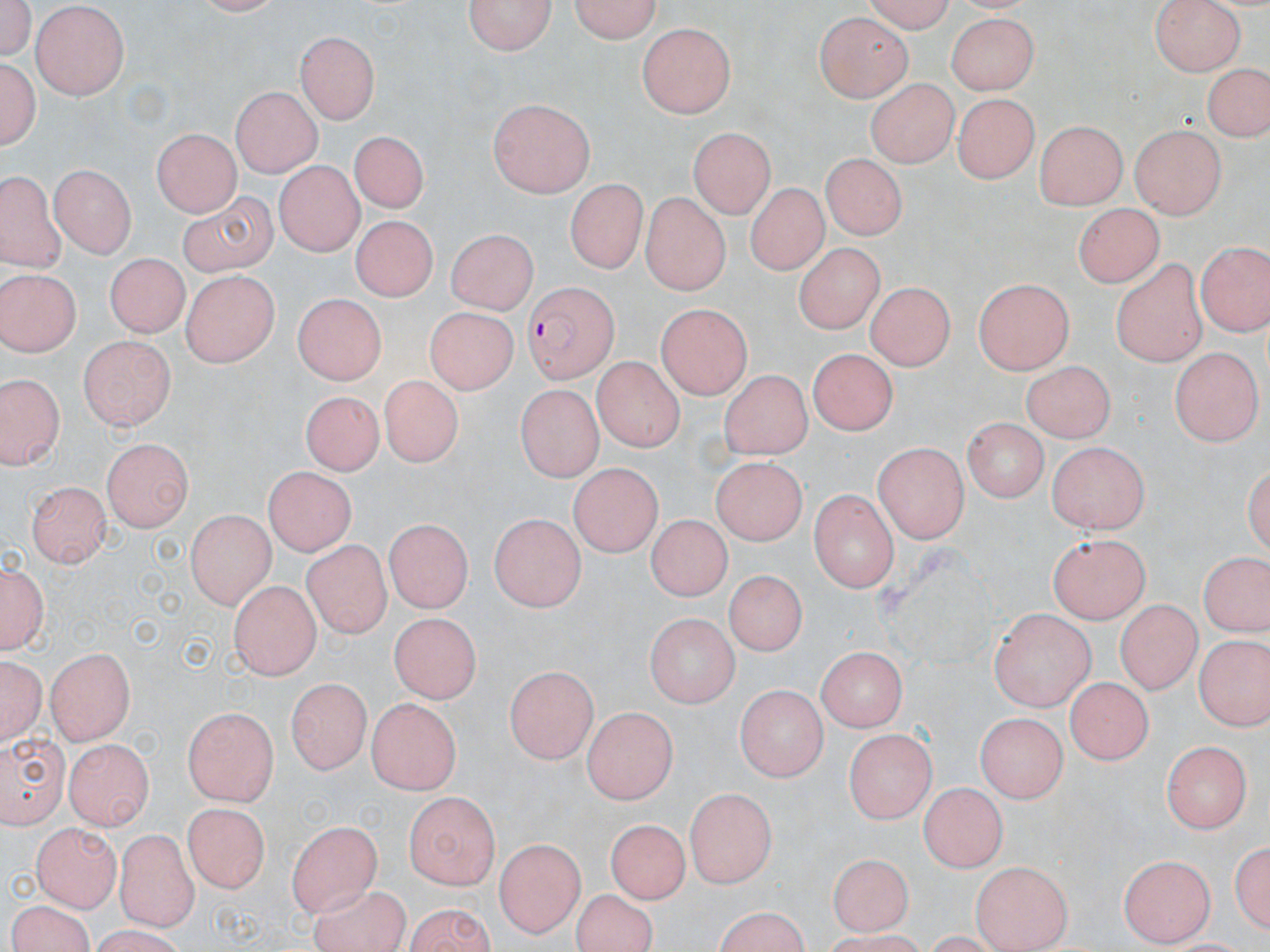

Summary:
  - Coordinate format: approximate bounding boxes as (x1,y1)-(x2,y2) corner pairs in pixels
  - Plasmodium falciparum-infected red blood cell locations: (523,282)-(617,384)
  - Uninfected red blood cell locations: (1,0)-(36,63), (467,0)-(555,57), (562,0)-(665,43), (858,0)-(958,29), (1150,0)-(1244,74), (32,5)-(134,100), (815,12)-(912,104), (944,13)-(1037,95), (637,26)-(737,119), (296,33)-(382,123), (2,56)-(40,154), (1207,61)-(1269,144), (866,76)-(956,167), (233,84)-(322,177), (956,94)-(1035,184), (489,100)-(597,199), (1036,121)-(1127,206), (1129,125)-(1229,219), (691,128)-(778,213), (149,129)-(241,216), (349,129)-(426,215), (823,153)-(905,243), (276,159)-(367,254), (50,165)-(136,258), (3,174)-(59,271), (566,178)-(646,274), (743,181)-(827,277), (172,190)-(278,277), (640,194)-(730,295), (1073,199)-(1161,290), (350,214)-(434,304), (445,230)-(543,313), (1196,238)-(1269,339), (795,242)-(882,334), (104,251)-(183,334), (1110,255)-(1208,365), (0,268)-(79,357), (175,273)-(278,367), (974,277)-(1072,375), (870,279)-(954,374), (292,294)-(386,384), (655,305)-(750,398), (422,307)-(519,395), (76,331)-(173,434), (1168,346)-(1260,446), (808,347)-(896,438), (595,355)-(688,451), (1020,360)-(1117,441), (719,371)-(813,459), (3,375)-(58,469), (377,375)-(459,471), (515,385)-(603,481), (299,390)-(388,476), (960,418)-(1049,503), (104,436)-(193,529), (1048,442)-(1148,536), (874,443)-(970,541), (713,457)-(811,545), (567,466)-(661,558), (263,468)-(355,554), (24,481)-(113,567), (806,486)-(901,592), (184,511)-(271,609), (489,512)-(587,609), (644,514)-(732,601), (384,519)-(470,611), (1049,534)-(1151,621), (305,537)-(397,634), (1198,549)-(1269,641), (2,556)-(48,655), (722,569)-(808,652), (230,577)-(318,679), (1118,600)-(1196,691), (990,607)-(1094,710), (389,611)-(481,703), (646,611)-(739,709), (1193,637)-(1267,729), (44,644)-(136,744), (813,645)-(908,730), (2,655)-(45,742), (504,666)-(596,763), (1068,675)-(1155,762), (284,679)-(371,775), (738,683)-(827,779), (365,698)-(458,795), (582,703)-(677,803), (182,706)-(278,805), (975,711)-(1069,804), (2,729)-(71,823), (844,729)-(935,824), (66,737)-(155,830), (1162,737)-(1253,832), (920,781)-(1007,872), (685,787)-(778,887), (401,792)-(503,885), (182,802)-(269,893), (607,816)-(688,904), (286,818)-(381,914), (33,824)-(119,910), (115,828)-(200,926), (1231,833)-(1269,933), (495,837)-(585,936), (828,848)-(912,936), (1122,854)-(1215,947), (970,860)-(1071,950), (305,883)-(407,952), (569,891)-(662,951), (5,900)-(100,952), (401,902)-(498,952), (709,909)-(815,952)
  - Slide-level diagnosis: Plasmodium falciparum
  - Image size: 1270×952 pixels
  - Preparation: thin blood smear
  - Field of view: single
  - Stain: May-Grünwald-Giemsa
  - Modality: light microscopy
  - Magnification: 1000x